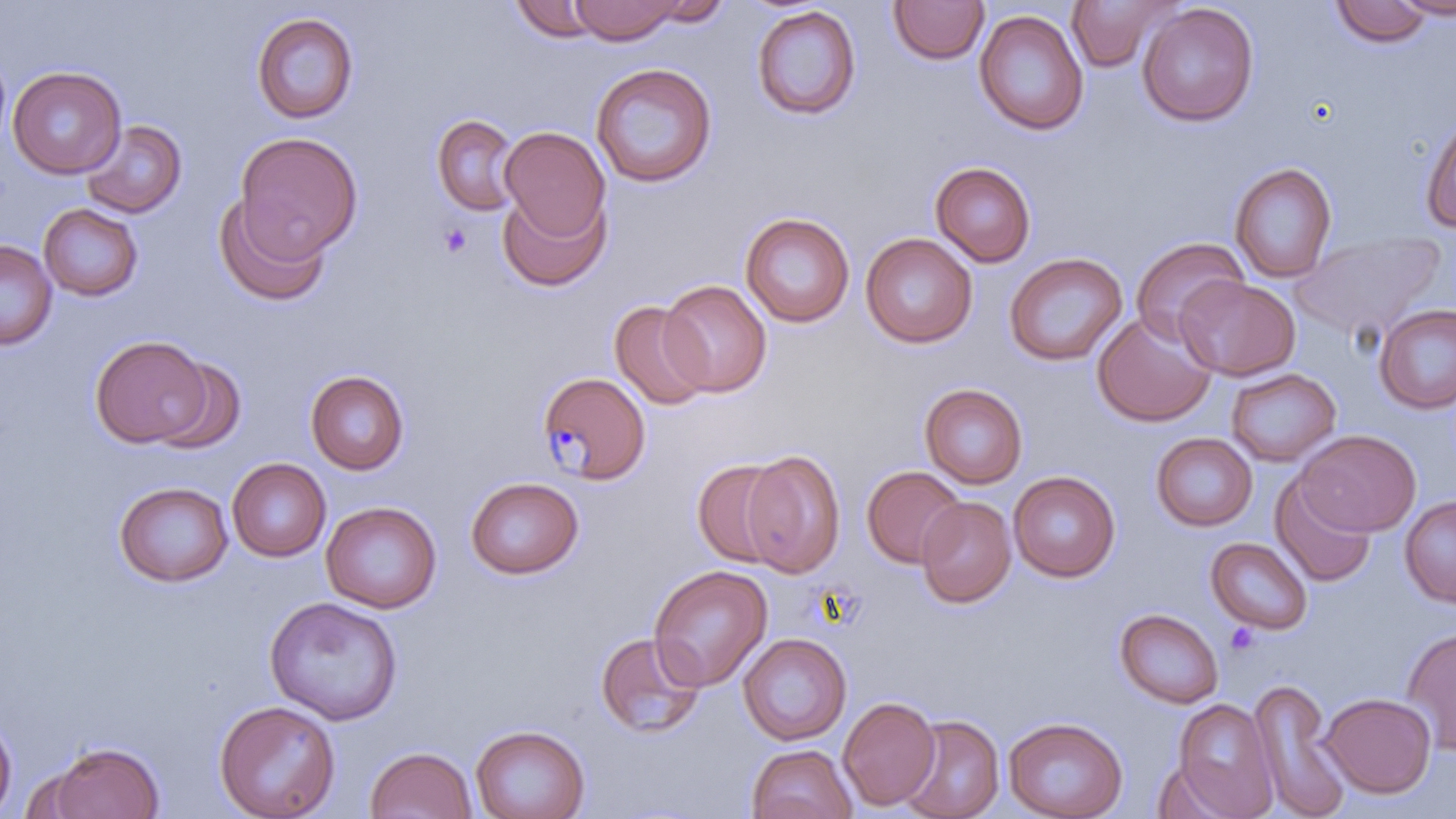
{
  "slide_level_diagnosis": "Plasmodium malariae",
  "image_size": "1456×819 pixels",
  "field_of_view": "single",
  "preparation": "thin blood film",
  "modality": "optical microscopy",
  "uninfected_red_blood_cell_locations": "approximate bounding boxes as (x1, y1, x2, y2) in pixels: (570, 0, 682, 44), (639, 0, 734, 28), (1066, 0, 1183, 73), (1392, 0, 1456, 19), (510, 1, 605, 42), (888, 1, 990, 65), (1330, 1, 1431, 47), (1137, 3, 1259, 127), (750, 5, 862, 121), (973, 9, 1089, 136), (250, 11, 359, 125), (0, 48, 12, 160), (590, 62, 718, 188), (8, 66, 126, 178), (1420, 112, 1456, 233), (431, 113, 523, 215), (80, 119, 186, 219), (499, 126, 611, 243), (234, 132, 363, 259), (930, 161, 1036, 267), (1229, 162, 1337, 284), (497, 184, 612, 292), (213, 191, 331, 307), (38, 203, 144, 301), (740, 212, 855, 327), (860, 232, 978, 348), (1292, 233, 1444, 341), (1130, 237, 1248, 344), (0, 240, 57, 350), (1003, 252, 1127, 367), (1174, 275, 1300, 380), (659, 280, 772, 397), (609, 300, 715, 411), (1372, 303, 1456, 414), (1091, 311, 1217, 427), (89, 334, 212, 449), (149, 356, 248, 454), (1225, 367, 1342, 467), (305, 370, 410, 475), (920, 383, 1028, 489), (1296, 428, 1421, 536), (1150, 432, 1257, 531), (740, 449, 846, 578), (227, 457, 331, 562), (692, 458, 792, 568), (862, 466, 966, 568), (1008, 471, 1121, 582), (1270, 474, 1377, 587), (465, 476, 584, 580), (113, 481, 233, 587), (1399, 495, 1456, 608), (916, 497, 1017, 609), (321, 500, 442, 613), (1205, 537, 1313, 635), (648, 565, 773, 691), (264, 596, 403, 725), (1114, 608, 1224, 709), (1401, 627, 1456, 754), (594, 631, 707, 740), (738, 633, 852, 745), (1247, 679, 1353, 818), (1320, 693, 1435, 798), (838, 696, 941, 810), (1172, 698, 1279, 817), (213, 699, 341, 819), (0, 712, 17, 816), (898, 714, 1004, 819), (1002, 717, 1129, 819), (470, 724, 591, 819), (47, 741, 166, 818), (746, 744, 858, 819), (365, 746, 477, 819), (1152, 759, 1243, 819)",
  "stain": "May-Grünwald-Giemsa",
  "magnification": "1000x",
  "platelet_locations": "approximate bounding boxes as (x1, y1, x2, y2) in pixels: (438, 223, 473, 257)",
  "plasmodium_malariae_infected_red_blood_cell_locations": "approximate bounding boxes as (x1, y1, x2, y2) in pixels: (537, 370, 651, 485)"
}